Identify the blood parasite species.
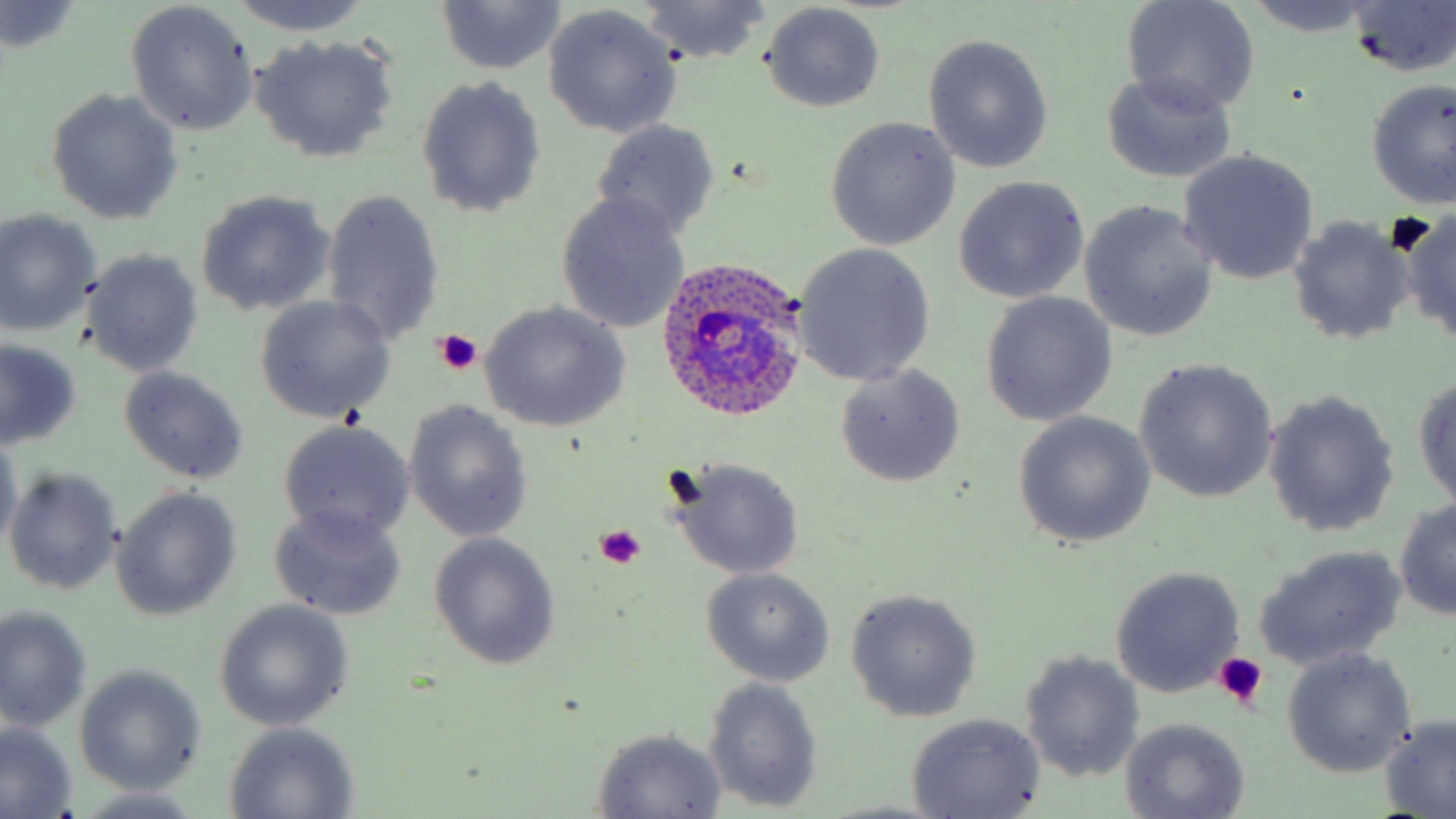
Plasmodium ovale.

preparation: thin blood smear
field_of_view: one of a larger specimen
plasmodium_ovale_infected_red_blood_cell_locations: 'approximate bounding boxes as named x1/y1/x2/y2 corners in pixels: (x1=655, y1=258, x2=815, y2=424)'
modality: optical microscopy
image_size: 1456×819 pixels
magnification: 1000x
stain: May-Grünwald-Giemsa
uninfected_red_blood_cell_locations: 'approximate bounding boxes as named x1/y1/x2/y2 corners in pixels: (x1=226, y1=0, x2=369, y2=36), (x1=634, y1=0, x2=773, y2=65), (x1=1245, y1=0, x2=1376, y2=35), (x1=1122, y1=1, x2=1261, y2=116), (x1=436, y1=2, x2=564, y2=75), (x1=1345, y1=2, x2=1456, y2=77), (x1=1, y1=3, x2=83, y2=53), (x1=126, y1=3, x2=258, y2=136), (x1=760, y1=3, x2=886, y2=111), (x1=543, y1=6, x2=681, y2=139), (x1=250, y1=34, x2=399, y2=163), (x1=923, y1=34, x2=1053, y2=173), (x1=1099, y1=70, x2=1238, y2=184), (x1=415, y1=76, x2=546, y2=219), (x1=1363, y1=79, x2=1455, y2=211), (x1=45, y1=90, x2=183, y2=225), (x1=824, y1=117, x2=960, y2=250), (x1=590, y1=118, x2=721, y2=241), (x1=1178, y1=151, x2=1318, y2=285), (x1=953, y1=177, x2=1089, y2=304), (x1=320, y1=188, x2=445, y2=349), (x1=195, y1=191, x2=335, y2=316), (x1=556, y1=195, x2=690, y2=333), (x1=1079, y1=199, x2=1219, y2=343), (x1=0, y1=209, x2=99, y2=334), (x1=1401, y1=210, x2=1456, y2=347), (x1=1286, y1=216, x2=1413, y2=346), (x1=792, y1=242, x2=936, y2=387), (x1=83, y1=250, x2=203, y2=376), (x1=980, y1=293, x2=1117, y2=427), (x1=254, y1=296, x2=396, y2=424), (x1=480, y1=302, x2=631, y2=433), (x1=0, y1=341, x2=80, y2=450), (x1=1133, y1=359, x2=1278, y2=504), (x1=835, y1=364, x2=966, y2=488), (x1=119, y1=366, x2=247, y2=483), (x1=1414, y1=372, x2=1456, y2=514), (x1=1263, y1=391, x2=1399, y2=537), (x1=402, y1=400, x2=535, y2=544), (x1=1012, y1=411, x2=1156, y2=549), (x1=278, y1=420, x2=415, y2=544), (x1=0, y1=432, x2=22, y2=551), (x1=665, y1=457, x2=807, y2=581), (x1=5, y1=466, x2=122, y2=595), (x1=110, y1=487, x2=241, y2=619), (x1=1392, y1=496, x2=1454, y2=619), (x1=269, y1=505, x2=406, y2=621), (x1=429, y1=532, x2=562, y2=670), (x1=1253, y1=545, x2=1405, y2=672), (x1=1109, y1=566, x2=1244, y2=699), (x1=700, y1=567, x2=836, y2=687), (x1=846, y1=589, x2=982, y2=722), (x1=212, y1=601, x2=353, y2=731), (x1=0, y1=606, x2=91, y2=731), (x1=1282, y1=649, x2=1416, y2=777), (x1=1019, y1=651, x2=1146, y2=781), (x1=73, y1=664, x2=207, y2=795), (x1=702, y1=678, x2=825, y2=813), (x1=904, y1=713, x2=1045, y2=819), (x1=1118, y1=717, x2=1251, y2=817), (x1=1378, y1=717, x2=1455, y2=816), (x1=0, y1=723, x2=78, y2=818), (x1=222, y1=723, x2=360, y2=817), (x1=589, y1=727, x2=728, y2=818), (x1=74, y1=789, x2=210, y2=818)'
platelet_locations: 'approximate bounding boxes as named x1/y1/x2/y2 corners in pixels: (x1=1386, y1=211, x2=1437, y2=259), (x1=433, y1=329, x2=483, y2=376), (x1=595, y1=527, x2=648, y2=570), (x1=1213, y1=653, x2=1267, y2=708)'